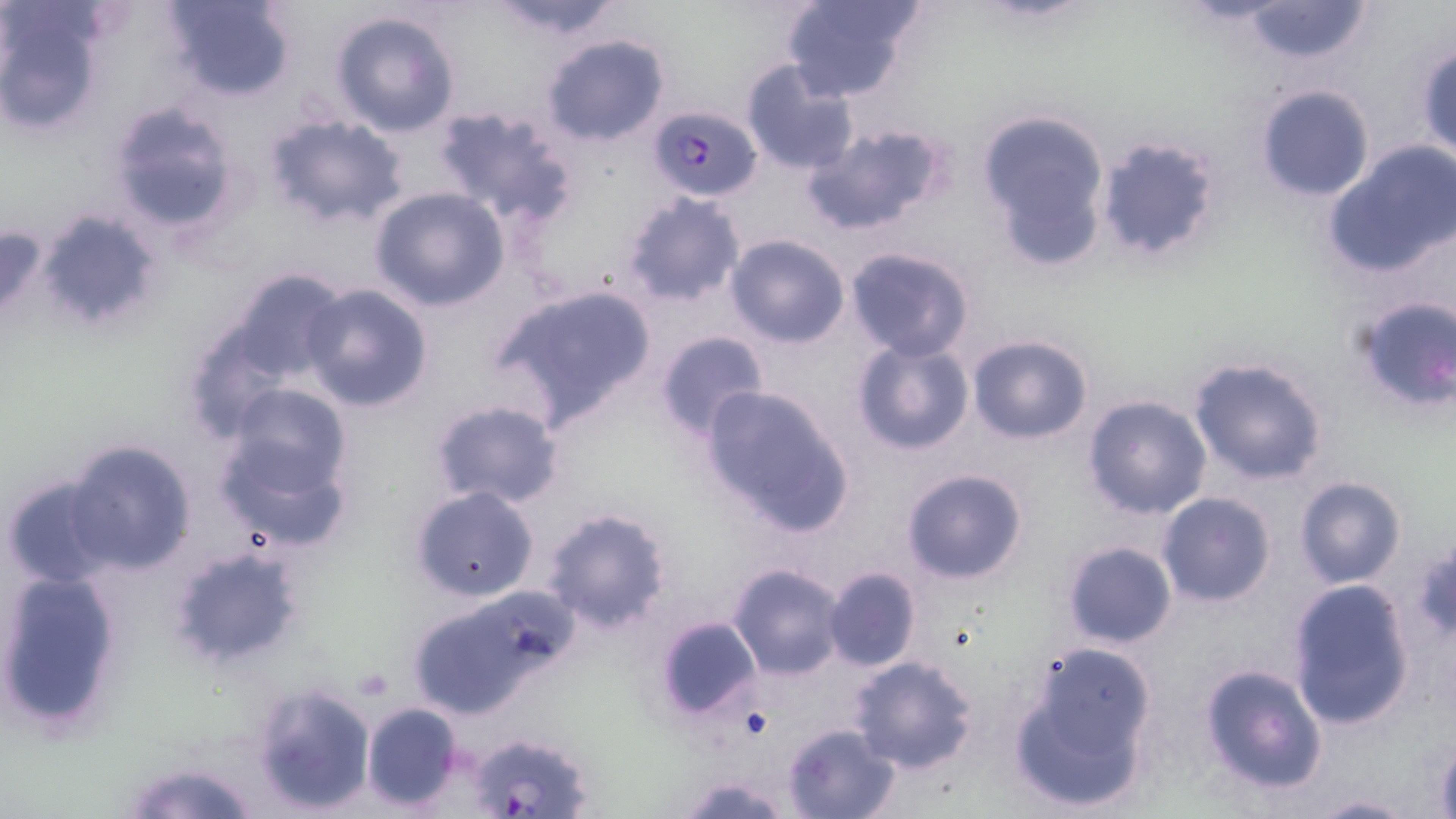 Approximate bounding boxes as (x1,y1)-(x2,y2) corner pairs in pixels. Uninfected red blood cell locations: (161,0)-(297,101), (488,0)-(628,44), (779,0)-(925,104), (1235,0)-(1376,66), (0,3)-(106,137), (328,10)-(460,138), (540,33)-(671,147), (1416,42)-(1455,161), (739,61)-(860,176), (1255,84)-(1375,203), (104,101)-(242,239), (434,104)-(579,225), (974,107)-(1111,269), (262,113)-(409,229), (803,121)-(951,236), (1094,135)-(1219,261), (1322,141)-(1456,280), (370,186)-(510,312), (622,193)-(747,308), (38,209)-(161,329), (724,234)-(851,349), (844,248)-(976,362), (223,268)-(348,386), (490,281)-(658,427), (301,282)-(434,412), (1348,294)-(1456,414), (653,330)-(770,442), (967,335)-(1093,442), (849,337)-(974,455), (1187,355)-(1330,485), (699,381)-(859,538), (221,382)-(357,521), (1083,395)-(1211,519), (430,398)-(565,510), (62,439)-(199,578), (901,468)-(1029,585), (2,475)-(115,589), (1295,477)-(1405,588), (410,485)-(540,603), (1156,492)-(1276,607), (540,505)-(673,634), (169,540)-(309,671), (1408,541)-(1456,644), (1062,542)-(1177,649), (728,562)-(848,679), (0,566)-(124,732), (823,567)-(920,672), (1287,579)-(1417,730), (406,599)-(542,719), (655,615)-(761,721), (1010,646)-(1156,813), (848,655)-(980,774), (1198,664)-(1326,794), (252,683)-(378,815), (361,703)-(462,810), (782,723)-(901,819), (1304,793)-(1415,818). Plasmodium falciparum-infected red blood cell locations: (648,104)-(762,201), (467,732)-(592,819). Slide-level diagnosis: Plasmodium falciparum. Optical microscopy. Thin blood film. Image is 1456×819 pixels. One field of a larger specimen. May-Grünwald-Giemsa stain. Captured at 1000x magnification.